Locate every Plasmodium parasite.
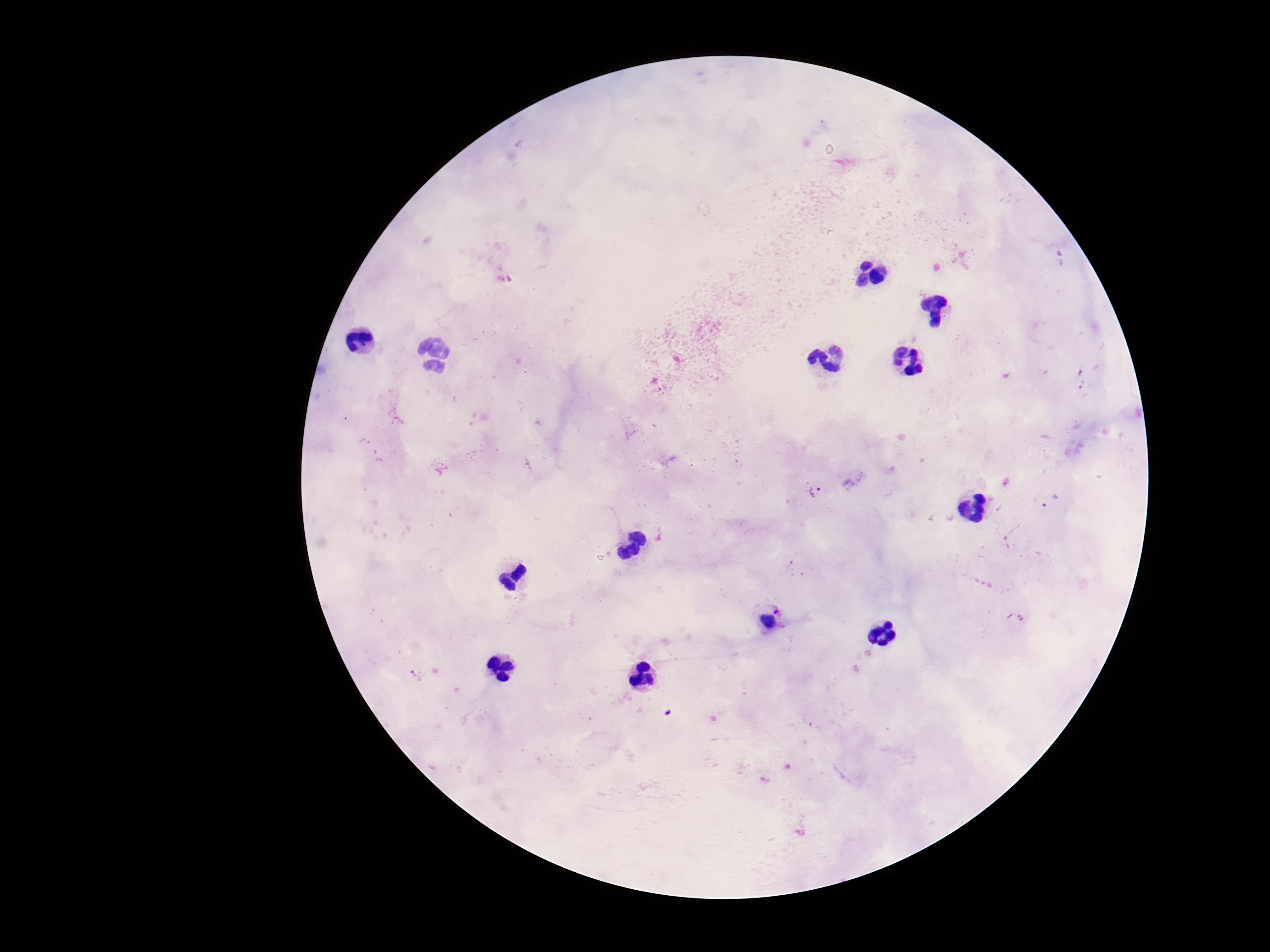

Approximate centers as [x, y] in pixels.
Plasmodium parasites: [820, 494], [779, 611].

{
  "patient_malaria_status": "infected",
  "image_size": "1270×952 pixels",
  "magnification": "100x",
  "preparation": "thick blood smear",
  "stain": "Giemsa",
  "capture": "smartphone camera through the microscope eyepiece",
  "field_of_view": "single"
}